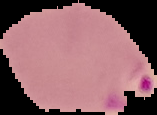
Summary:
  - Preparation: thin blood smear
  - Malaria status: parasitized
  - Image type: cell region segmented out of the field of view; surrounding area masked to black
  - Image size: 157×115 pixels